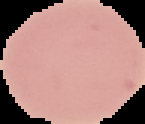
preparation = thin blood film
malaria status = uninfected
image type = cell region segmented out of the field of view; surrounding area masked to black
image size = 145×124 pixels